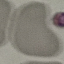

Summary:
  - Malaria status: uninfected
  - Stain: Giemsa
  - Image type: cell patch, automatically extracted from a larger field of view and resized to 64 × 64 pixels
  - Capture: smartphone camera at the microscope eyepiece
  - Preparation: thin blood film